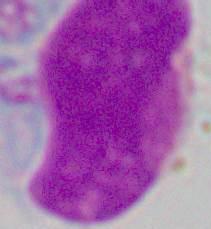

Summary:
  - Identification: leukocyte
  - Magnification: 1000x
  - Modality: photomicrograph